Outline every malaria parasite, every leukocyte, and every artifact (stain precipitate or debris).
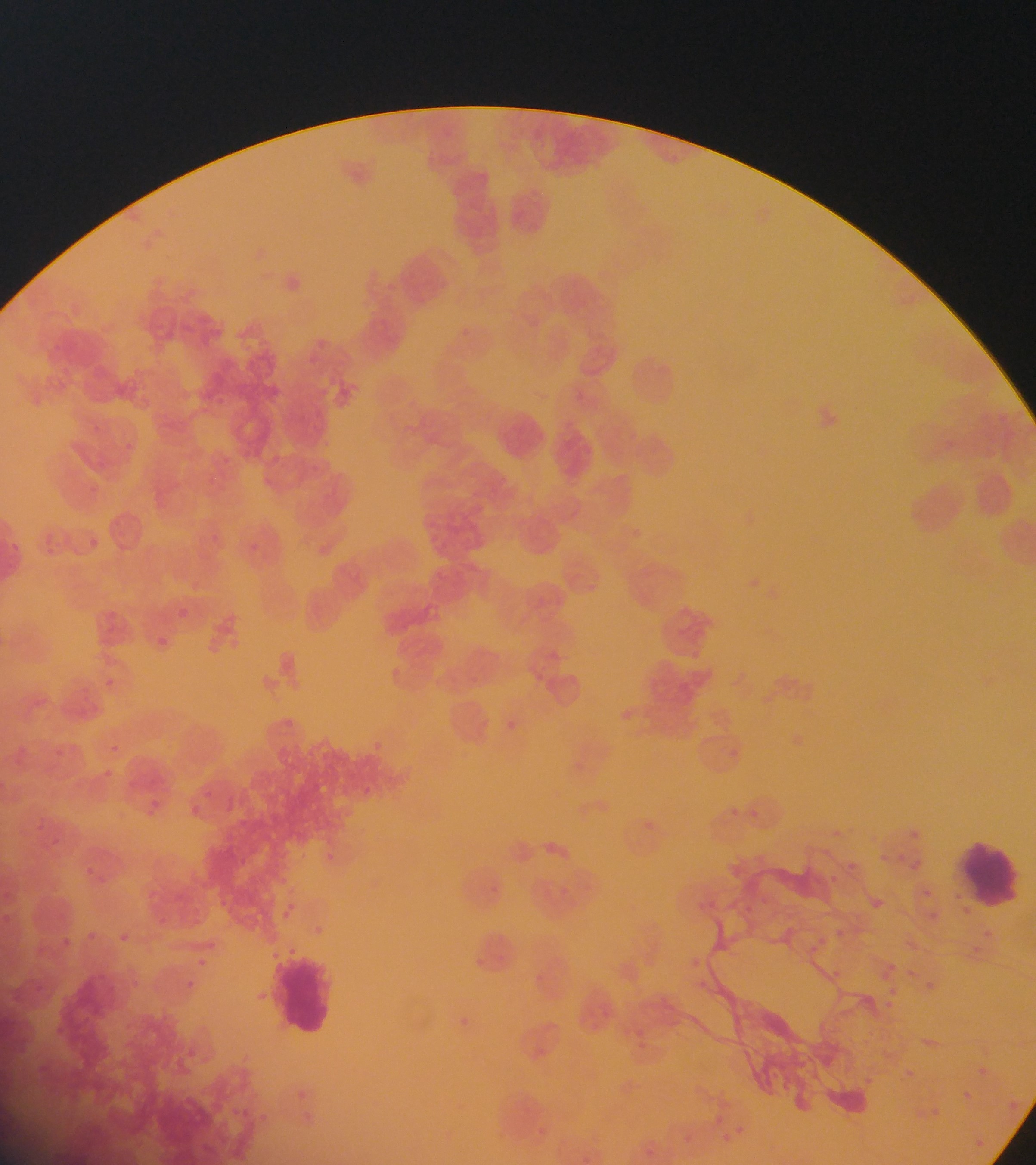

Approximate bounding boxes as (left, top, right, bottom) in pixels.
Malaria parasites: (453, 325, 472, 342), (747, 573, 762, 589), (176, 592, 195, 617), (157, 635, 177, 662), (618, 704, 643, 724), (101, 724, 133, 752), (103, 770, 145, 813), (225, 798, 248, 816), (172, 799, 212, 832), (735, 803, 741, 815), (751, 808, 773, 822), (909, 827, 939, 849), (894, 851, 904, 858), (910, 855, 932, 872), (841, 856, 862, 876), (823, 870, 842, 889), (924, 886, 935, 901), (864, 894, 887, 915), (932, 909, 944, 925), (833, 926, 847, 940), (111, 930, 132, 949), (914, 936, 928, 955), (193, 955, 209, 969), (886, 961, 900, 975), (181, 977, 198, 993), (888, 978, 906, 1000), (921, 978, 938, 995), (883, 997, 894, 1014), (900, 1062, 935, 1088), (970, 1063, 991, 1082), (861, 1071, 875, 1081), (956, 1087, 974, 1105), (937, 1104, 946, 1116), (739, 1119, 754, 1142), (722, 1130, 736, 1145), (968, 1135, 988, 1153) | approximate (x, y) pixel centers of objects too small to bound: (811, 950).
Leukocytes: (492, 409, 551, 468), (956, 842, 1023, 910), (274, 954, 339, 1038).

{
  "image_size": "1036×1165 pixels",
  "capture": "mobile-phone photograph through a microscope",
  "country": "Ghana",
  "field_of_view": "single",
  "preparation": "thin blood film"
}